Assess this cell for malaria.
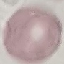
Uninfected.

Summary:
  - Image type: automatically extracted cell patch, resized to 64 × 64 pixels
  - Capture: smartphone camera at the microscope eyepiece
  - Preparation: thin smear
  - Stain: Giemsa